Locate every blood parasite and identify its species.
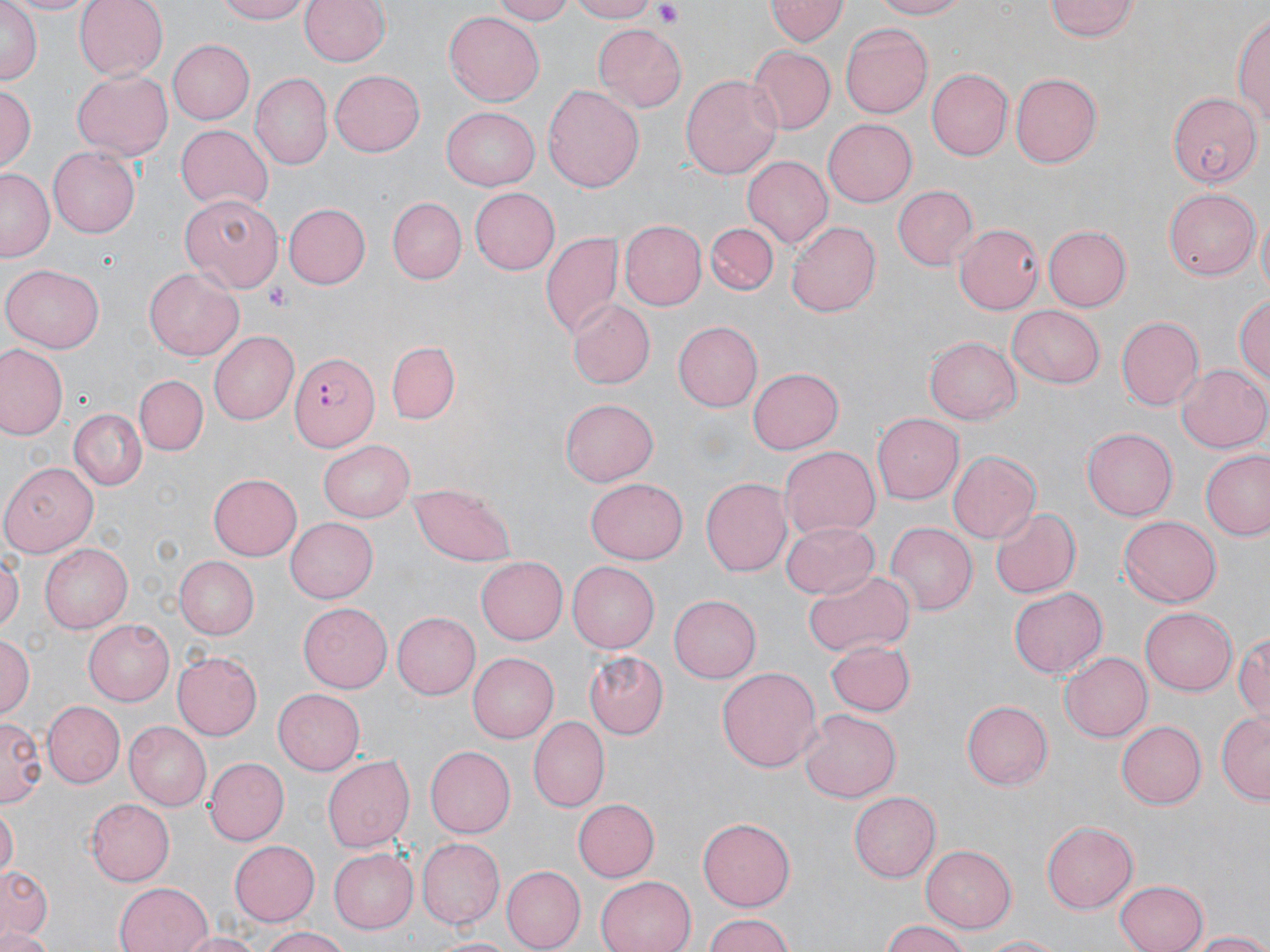
Approximate bounding boxes as (x1,y1)-(x2,y2) corner pairs in pixels.
Plasmodium falciparum-infected red blood cells: (290,348)-(381,450).
No Plasmodium ovale, Plasmodium malariae, Plasmodium vivax, Babesia divergens, or Trypanosoma brucei observed.

Summary:
  - Uninfected red blood cell locations: (2,0)-(96,17), (73,0)-(167,79), (214,0)-(315,24), (298,0)-(389,69), (488,0)-(577,24), (565,0)-(661,23), (867,0)-(967,20), (1,1)-(40,89), (765,1)-(848,46), (1044,1)-(1140,43), (1235,9)-(1269,128), (444,12)-(546,106), (840,22)-(934,119), (595,25)-(687,112), (168,40)-(254,123), (745,46)-(836,134), (929,69)-(1012,162), (71,70)-(172,161), (330,70)-(425,157), (678,72)-(784,180), (250,73)-(333,171), (1009,73)-(1100,169), (1,82)-(37,174), (543,84)-(644,192), (443,105)-(541,190), (823,121)-(916,207), (175,124)-(273,214), (46,146)-(141,239), (741,156)-(833,248), (0,169)-(53,261), (468,186)-(560,274), (893,186)-(977,270), (1164,188)-(1260,281), (179,193)-(281,294), (387,199)-(465,284), (282,202)-(369,289), (1256,213)-(1269,295), (619,219)-(706,311), (787,221)-(879,315), (706,223)-(778,295), (954,225)-(1041,312), (1042,225)-(1130,312), (542,231)-(623,339), (3,263)-(105,351), (145,268)-(244,361), (1236,290)-(1270,394), (565,299)-(653,390), (1006,305)-(1105,389), (1116,316)-(1203,410), (673,320)-(762,411), (209,331)-(299,425), (925,336)-(1022,424), (387,342)-(459,423), (0,345)-(65,439), (747,364)-(843,456), (1176,364)-(1270,455), (135,376)-(207,454), (560,398)-(658,486), (70,409)-(144,490), (872,413)-(963,504), (1082,427)-(1179,520), (320,439)-(416,521), (779,445)-(880,538), (947,451)-(1039,545), (1202,451)-(1270,540), (0,463)-(102,559), (207,472)-(302,562), (585,477)-(689,564), (701,477)-(793,576), (410,483)-(515,565), (991,506)-(1081,599), (285,516)-(378,603), (1118,516)-(1220,607), (782,519)-(880,600), (884,522)-(975,616), (40,541)-(133,630), (0,551)-(22,636), (171,555)-(258,639), (476,557)-(567,645), (567,561)-(659,652), (804,570)-(913,656), (1009,587)-(1108,679), (670,592)-(763,682), (297,603)-(392,694), (1140,608)-(1235,695), (392,611)-(481,699), (82,618)-(174,705), (1234,631)-(1270,724), (1,632)-(34,722), (823,639)-(914,717), (171,651)-(262,742), (1058,651)-(1150,742), (468,652)-(558,742), (583,653)-(668,741), (716,666)-(821,773), (273,690)-(364,774), (962,697)-(1052,788), (44,701)-(124,786), (799,709)-(901,802), (1216,712)-(1270,804), (0,715)-(43,808), (529,717)-(609,810), (123,722)-(210,810), (1117,722)-(1206,809), (422,746)-(514,839), (323,754)-(415,853), (203,756)-(289,846), (209,758)-(307,916), (849,790)-(941,882), (85,798)-(175,885), (571,798)-(657,883), (0,807)-(18,874), (699,816)-(797,910), (1041,822)-(1136,914), (418,837)-(506,928), (230,839)-(321,925), (918,844)-(1018,932), (329,849)-(419,934), (1,864)-(51,941), (502,867)-(584,950), (594,877)-(693,952), (1113,879)-(1208,952), (114,881)-(213,952), (700,914)-(794,951), (878,919)-(972,952), (259,927)-(353,952), (0,928)-(55,952), (177,931)-(261,952), (1188,931)-(1270,951), (427,934)-(519,951), (973,935)-(1065,952)
  - Platelet locations: (653,3)-(686,29), (267,283)-(292,311)
  - Slide-level diagnosis: Plasmodium falciparum
  - Image size: 1270×952 pixels
  - Field of view: single
  - Modality: optical microscopy
  - Magnification: 1000x
  - Preparation: thin blood smear
  - Stain: May-Grünwald-Giemsa